Locate every Plasmodium parasite and every leukocyte.
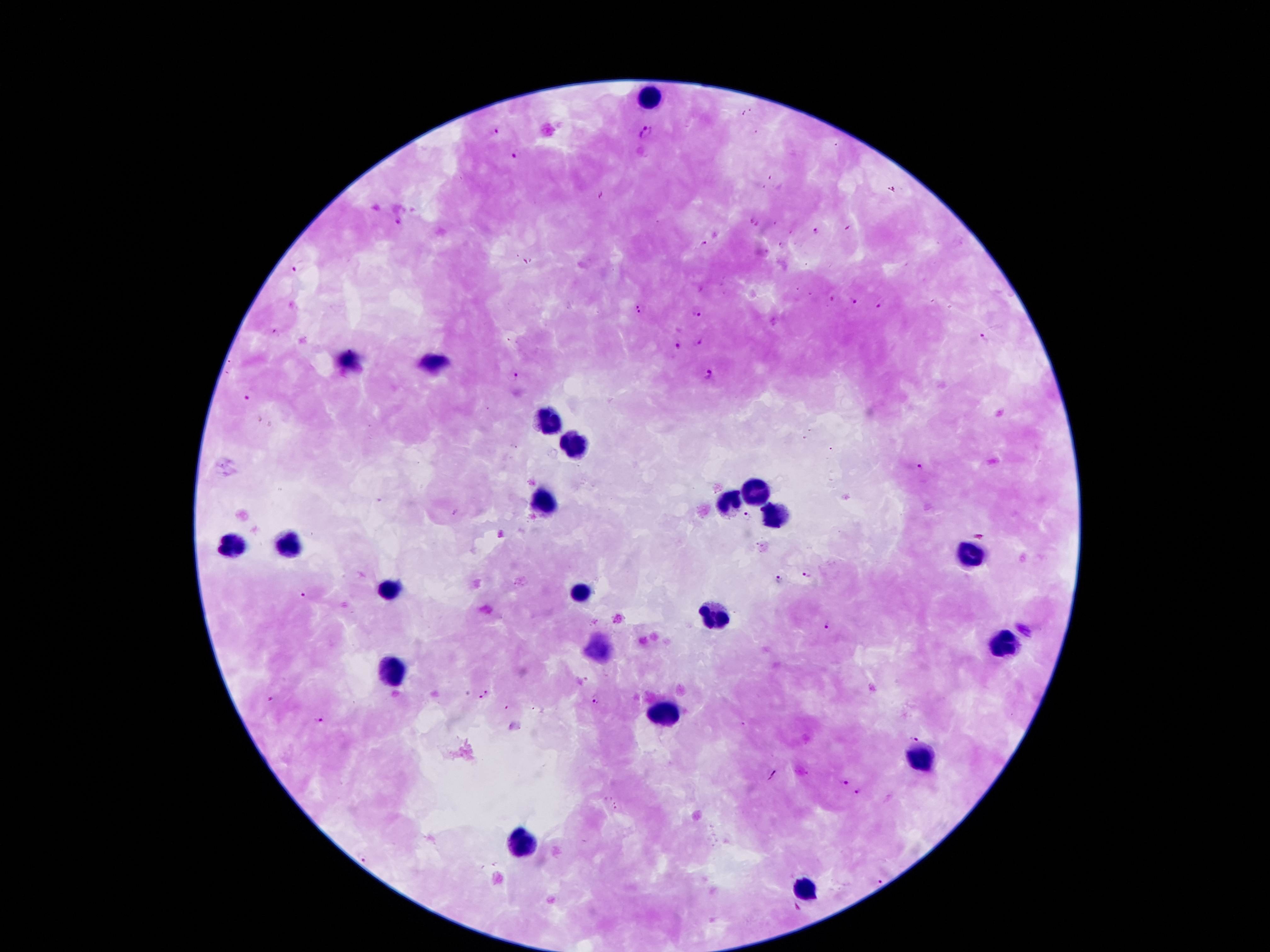

Approximate centers as {x, y} in pixels.
Plasmodium parasites: {644, 132}, {496, 133}, {516, 151}, {895, 188}, {750, 220}, {398, 221}, {759, 225}, {817, 231}, {703, 244}, {299, 264}, {831, 299}, {854, 301}, {878, 305}, {639, 306}, {698, 313}, {274, 332}, {984, 338}, {698, 342}, {677, 344}, {710, 374}, {513, 376}, {250, 394}, {920, 468}, {749, 512}, {807, 575}, {778, 576}, {303, 594}, {826, 627}, {488, 693}, {271, 694}, {594, 698}, {507, 706}, {321, 717}, {914, 735}, {844, 781}, {859, 790}, {364, 858}, {880, 879}.
Leukocytes: {647, 99}, {349, 362}, {431, 367}, {547, 424}, {574, 448}, {755, 491}, {544, 501}, {726, 503}, {776, 517}, {290, 542}, {231, 544}, {973, 553}, {387, 589}, {583, 591}, {717, 617}, {1007, 642}, {597, 648}, {390, 675}, {665, 714}, {923, 758}, {522, 841}, {803, 891}.

{
  "stain": "Giemsa",
  "field_of_view": "single",
  "magnification": "100x",
  "patient_malaria_status": "infected with Plasmodium falciparum",
  "image_size": "1270×952 pixels",
  "preparation": "thick peripheral-blood smear",
  "capture": "smartphone camera through the microscope eyepiece"
}